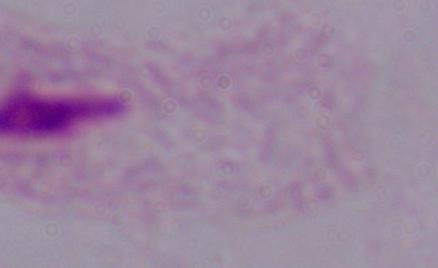 Photomicrograph. Captured at 1000x magnification. A trichomonad is shown.